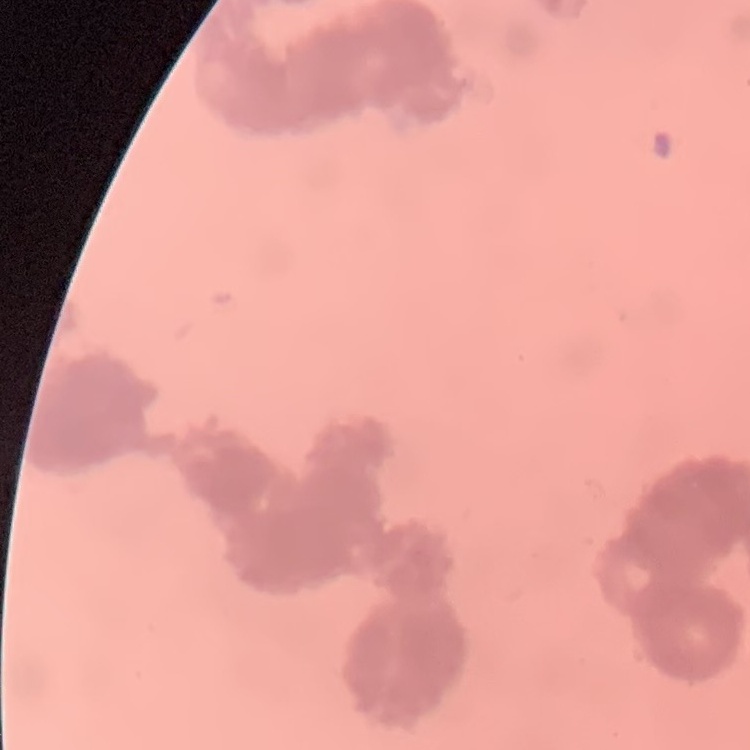

erythrocyte morphology = rouleaux formation
image type = square crop of a larger photomicrograph
stain = Field's or Giemsa
preparation = thin peripheral smear